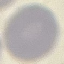

result = no malaria parasites detected
capture = smartphone through the microscope eyepiece
image type = cell patch, automatically extracted from a larger field of view and resized to 64 × 64 pixels
stain = Giemsa
preparation = thin blood film